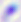 Captured at 400x magnification. Photomicrograph. Toxoplasma gondii is shown.